Point out every malaria parasite and every leukocyte.
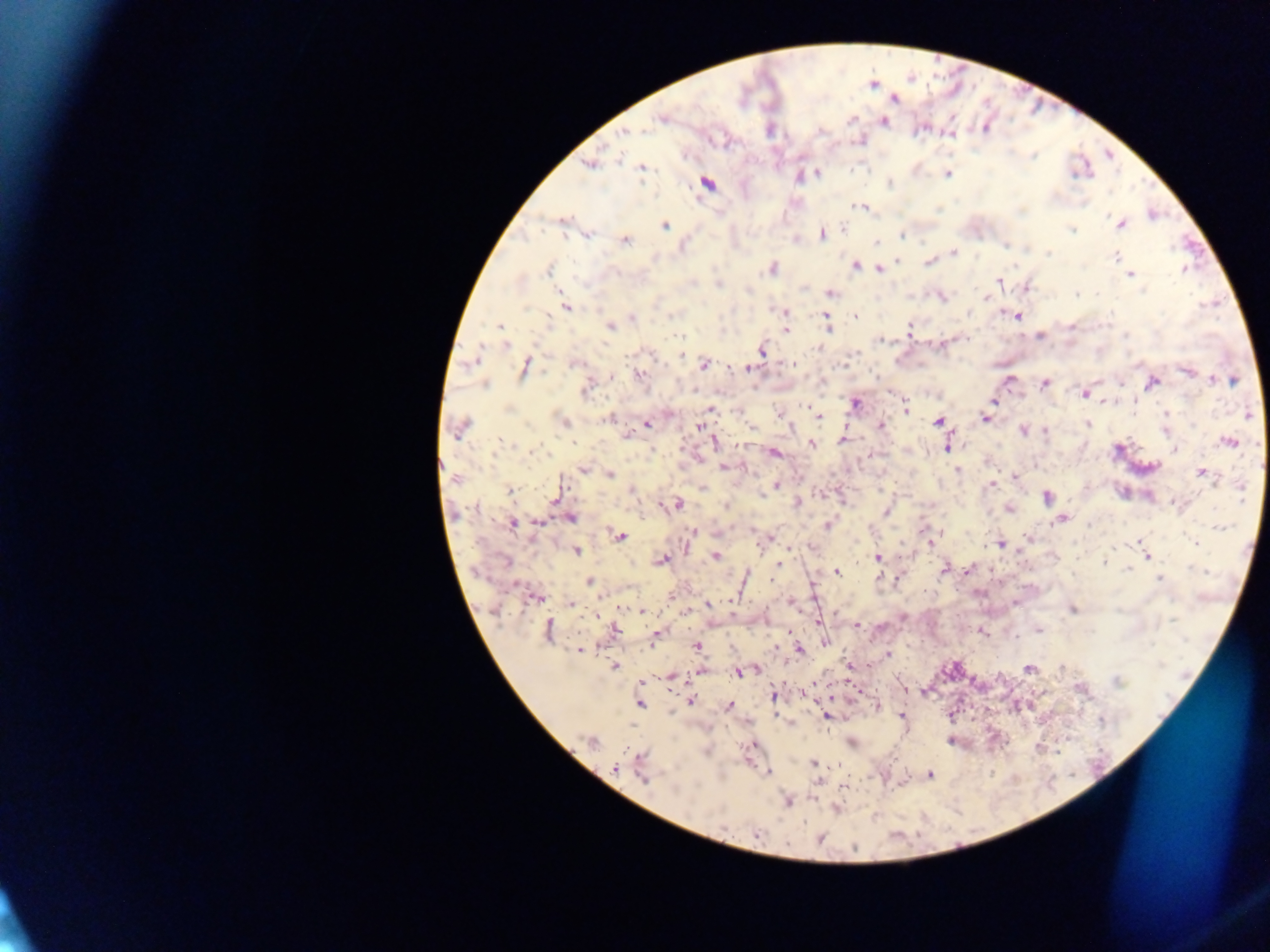

Approximate centers as [x, y] in pixels.
Malaria parasites: [893, 99], [661, 119], [884, 121], [820, 132], [623, 133], [588, 164], [642, 168], [817, 173], [948, 174], [707, 183], [889, 183], [855, 206], [862, 207], [1152, 214], [563, 222], [1121, 224], [665, 225], [843, 228], [1071, 230], [822, 234], [588, 236], [901, 236], [626, 240], [876, 242], [1006, 245], [953, 253], [1049, 253], [1116, 256], [898, 261], [929, 262], [856, 266], [773, 268], [1184, 269], [549, 270], [879, 270], [1130, 274], [999, 280], [718, 285], [1027, 287], [830, 293], [1077, 294], [941, 298], [987, 298], [566, 307], [782, 311], [968, 314], [824, 316], [855, 316], [1017, 316], [671, 317], [632, 318], [499, 326], [610, 326], [1071, 326], [827, 327], [909, 329], [786, 330], [680, 336], [1040, 336], [1126, 336], [506, 345], [819, 348], [762, 350], [682, 355], [793, 363], [576, 364], [703, 365], [524, 368], [749, 368], [1186, 371], [612, 375], [639, 375], [1009, 380], [1212, 380], [1233, 380], [1045, 383], [1152, 383], [484, 384], [586, 388], [1083, 395], [995, 401], [855, 404], [808, 407], [711, 409], [906, 409], [1248, 414], [819, 417], [985, 418], [607, 420], [564, 421], [938, 422], [1089, 423], [646, 424], [881, 426], [699, 427], [751, 427], [459, 429], [1023, 430], [1165, 430], [1045, 431], [627, 434], [843, 440], [715, 441], [500, 442], [1230, 442], [511, 444], [812, 444], [948, 446], [1174, 450], [774, 453], [723, 467], [582, 470], [957, 470], [1204, 473], [610, 475], [1017, 478], [455, 479], [992, 484], [777, 486], [703, 489], [509, 491], [631, 491], [1242, 491], [556, 498], [1047, 498], [797, 504], [677, 505], [726, 507], [1010, 509], [886, 511], [570, 518], [1061, 519], [512, 523], [539, 523], [829, 524], [1223, 527], [692, 532], [619, 536], [1028, 538], [929, 539], [1194, 542], [1001, 544], [576, 552], [1146, 555], [715, 556], [878, 557], [661, 560], [1104, 561], [778, 565], [967, 569], [1127, 569], [944, 570], [1200, 570], [836, 572], [1159, 579], [589, 582], [535, 597], [791, 602], [571, 604], [709, 605], [1073, 609], [642, 611], [1172, 619], [857, 625], [1038, 630], [548, 631], [615, 631], [982, 632], [657, 635], [825, 642], [698, 645], [799, 649], [580, 650], [888, 655], [614, 666], [849, 666], [1029, 668], [701, 671], [739, 672], [672, 677], [1117, 682], [773, 696], [690, 701], [640, 704], [729, 705], [875, 706], [902, 715], [827, 716], [1102, 721], [591, 742], [852, 743], [813, 762], [614, 767], [768, 773], [929, 775], [643, 778], [788, 801], [756, 833], [820, 839].
No leukocytes observed.

Summary:
  - Capture: mobile-phone photograph through a microscope
  - Image size: 1270×952 pixels
  - Country: Ghana
  - Field of view: single
  - Preparation: thick blood smear